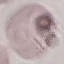

result = no malaria parasites detected
capture = smartphone camera at the microscope eyepiece
preparation = thin blood smear
stain = Giemsa
image type = automatically extracted cell patch, resized to 64 × 64 pixels